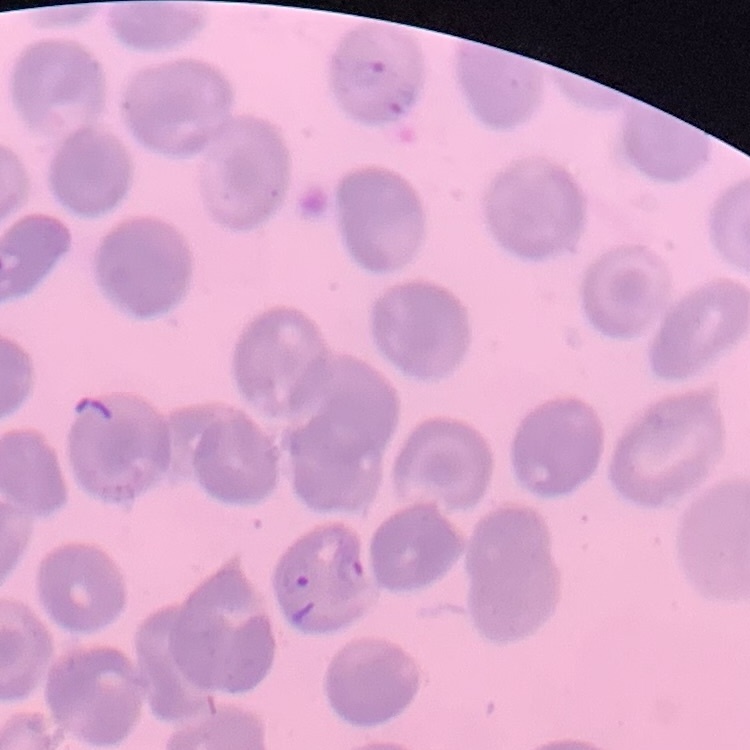

The red blood cells exhibit no rouleaux formation. Thin blood film. Stained with either Field's or Giemsa. Square crop of a larger photomicrograph.